State which parasite is depicted.
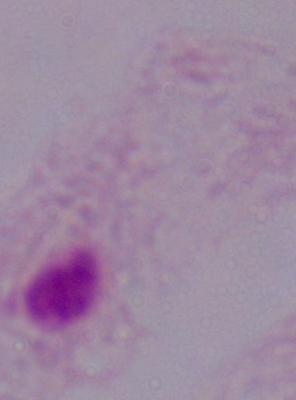

This is a trichomonad.

Summary:
  - Modality: micrograph
  - Magnification: 1000x